Locate every blood parasite and identify its species.
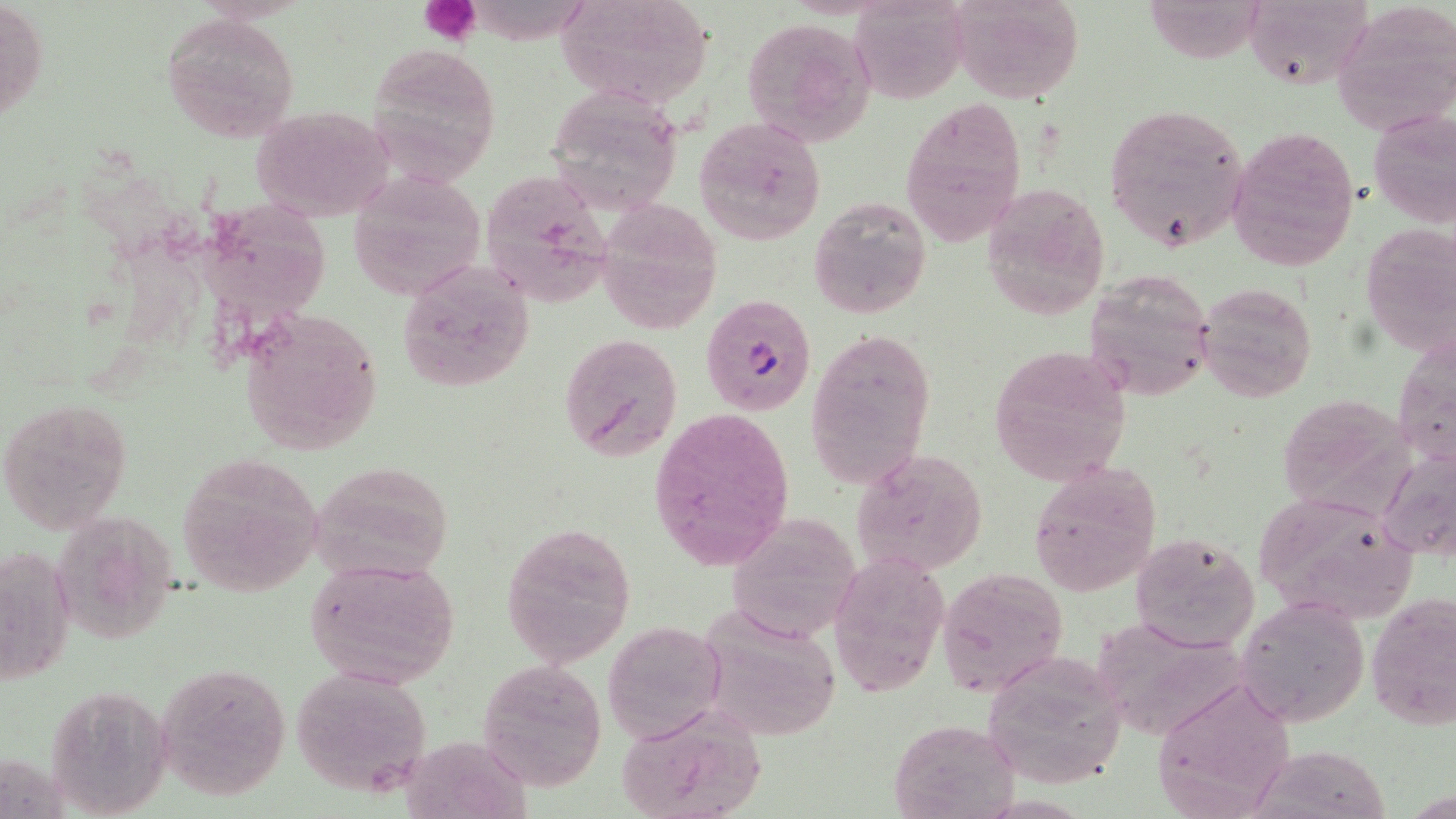
Approximate bounding boxes as (x1,y1)-(x2,y2) corner pairs in pixels.
Plasmodium falciparum-infected red blood cells: (700,293)-(817,417).
No Plasmodium ovale, Plasmodium malariae, Plasmodium vivax, Babesia divergens, or Trypanosoma brucei observed.

Summary:
  - Uninfected red blood cell locations: (1,0)-(49,129), (552,0)-(716,112), (849,0)-(969,104), (947,0)-(1085,104), (1243,0)-(1372,91), (1333,5)-(1455,138), (160,14)-(301,143), (741,18)-(878,146), (367,41)-(501,183), (558,92)-(677,213), (901,97)-(1026,247), (1103,102)-(1249,253), (249,106)-(393,220), (1368,107)-(1456,229), (694,116)-(827,245), (1227,125)-(1361,273), (348,170)-(487,301), (482,173)-(615,311), (979,184)-(1109,321), (202,192)-(331,327), (809,193)-(931,318), (598,199)-(724,330), (1360,224)-(1454,355), (394,258)-(535,394), (1083,270)-(1217,403), (1198,281)-(1316,402), (238,307)-(385,457), (805,327)-(935,489), (559,331)-(685,464), (988,345)-(1133,484), (1276,393)-(1414,515), (0,396)-(134,536), (648,406)-(795,572), (1378,446)-(1456,561), (853,449)-(988,574), (176,454)-(325,598), (310,461)-(458,586), (1028,461)-(1161,595), (1251,491)-(1421,625), (722,514)-(861,644), (502,521)-(636,667), (1129,531)-(1260,653), (2,543)-(78,686), (829,550)-(950,698), (304,556)-(460,689), (936,566)-(1069,698), (1366,590)-(1456,734), (1235,597)-(1369,728), (693,606)-(844,744), (1087,617)-(1253,741), (602,619)-(727,744), (980,653)-(1128,789), (477,658)-(607,793), (157,661)-(292,798), (289,665)-(434,798), (1152,674)-(1299,816), (614,704)-(769,819), (887,717)-(1020,818)
  - Platelet locations: (418,0)-(483,45)
  - Slide-level diagnosis: Plasmodium falciparum
  - Magnification: 1000x
  - Preparation: thin blood film
  - Field of view: one of a larger specimen
  - Modality: optical microscopy
  - Image size: 1456×819 pixels
  - Stain: May-Grünwald-Giemsa